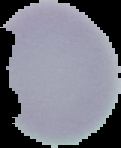

{
  "image_type": "cell region segmented out of the field of view; surrounding area masked to black",
  "result": "negative for malaria parasites",
  "image_size": "121×148 pixels",
  "preparation": "thin blood smear"
}